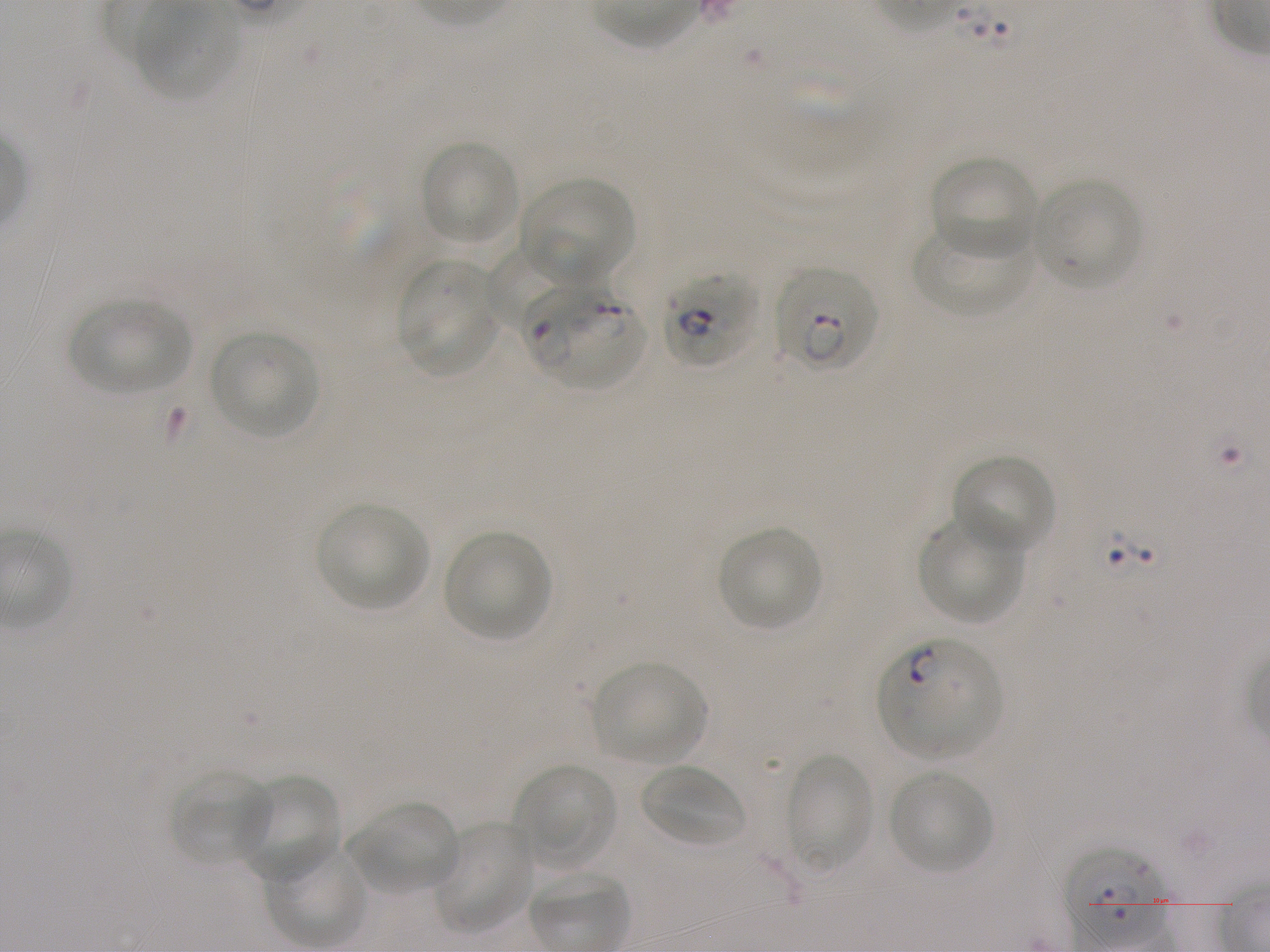
Approximate bounding boxes as (x1, y1, x2, y2) in pixels. Not every red blood cell is marked. A life-cycle stage — or a range of stages, where the recorded stages span more than one — follows each staged infected red blood cell.
Summary:
  - Locations of uninfected red blood cells: (133, 2, 241, 101), (419, 139, 519, 245), (929, 155, 1038, 258), (520, 178, 635, 284), (1033, 179, 1143, 289), (911, 221, 1035, 317), (483, 244, 569, 330), (396, 258, 500, 376), (68, 298, 192, 395), (209, 331, 319, 439), (952, 454, 1056, 556), (317, 503, 429, 611), (917, 512, 1025, 626), (717, 526, 823, 632), (443, 530, 552, 641), (590, 660, 708, 765), (783, 753, 875, 873), (513, 763, 619, 869), (639, 765, 746, 849), (169, 768, 275, 867), (888, 769, 996, 875), (236, 774, 339, 886), (346, 800, 462, 895), (430, 821, 535, 932), (266, 842, 369, 949)
  - Locations of infected red blood cells: (773, 267, 880, 374) early ring to early trophozoite; (660, 270, 758, 369) late ring to early trophozoite; (527, 287, 646, 390); (877, 636, 1002, 761) ring; (1066, 853, 1166, 943) ring
  - Image size: 1270×952 pixels
  - Field of view: one from this slide
  - Culture: in-vitro P. falciparum strain NF54, static
  - Stain: Giemsa
  - Objective: 100x, oil immersion, numerical aperture 1.25
  - Donor blood group: A+
  - Preparation: thin blood smear